Report the malaria status of this cell.
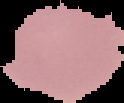
It is uninfected.

{
  "image_type": "cell region segmented out of the field of view; surrounding area masked to black",
  "preparation": "thin blood film",
  "image_size": "124×103 pixels"
}